State the preparation type.
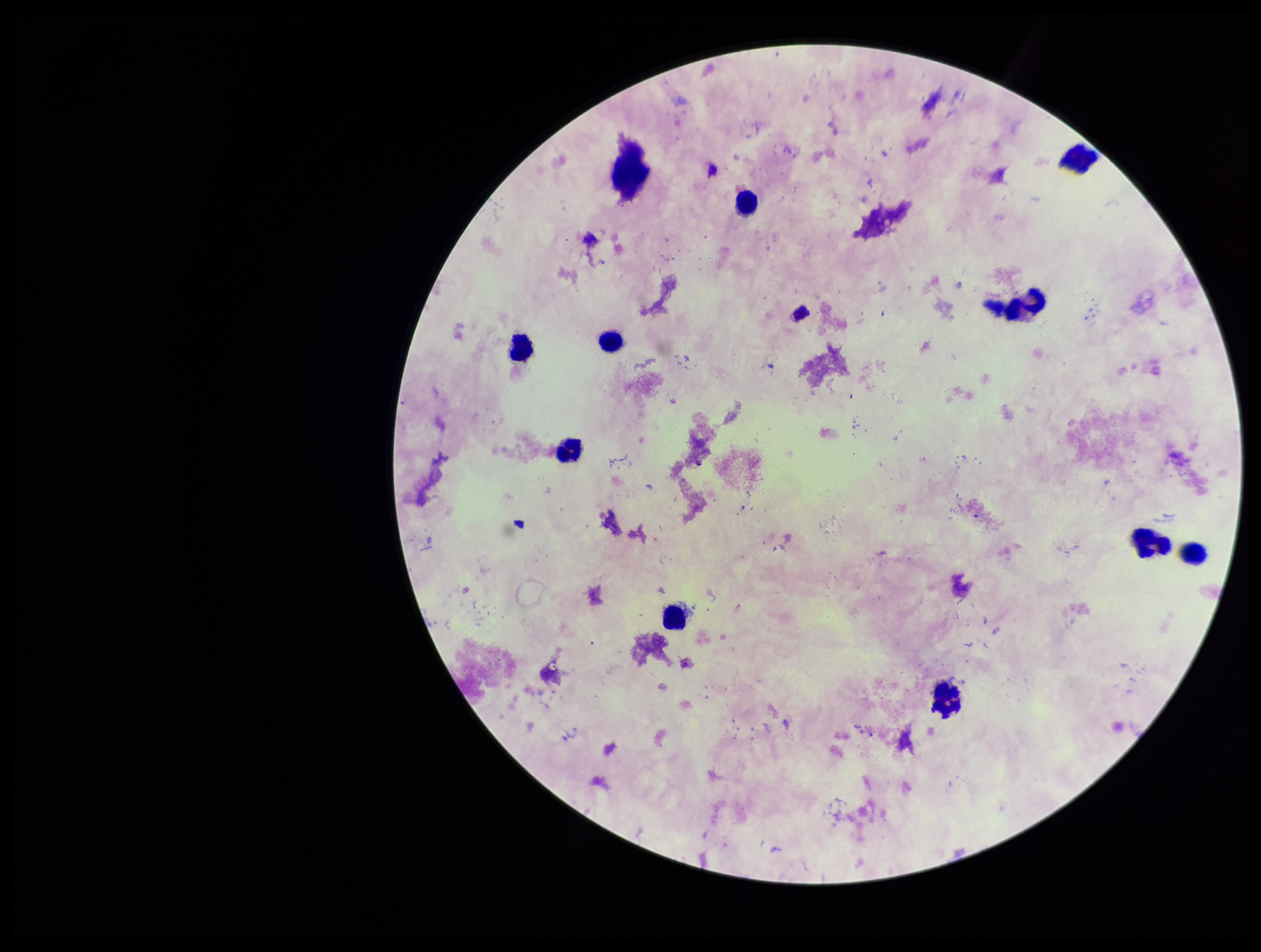
A thick smear.

Summary:
  - Leukocyte count: 10
  - Patient malaria status: negative
  - Parasite count: 0
  - Stain: Giemsa
  - Image size: 1261×952 pixels
  - Capture: smartphone photograph through the microscope eyepiece
  - Field of view: single
  - Plasmodium parasites: none seen